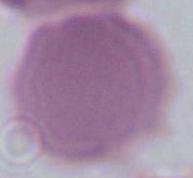

modality = photomicrograph
magnification = 1000x
identification = erythrocyte